Report the malaria status of this cell.
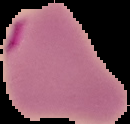

Parasitized.

image_size: 130×124 pixels
preparation: thin blood smear
image_type: cell region segmented out of the field of view; surrounding area masked to black